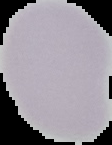
Summary:
  - Image size: 112×145 pixels
  - Preparation: thin blood film
  - Image type: cell region segmented out of the field of view; surrounding area masked to black
  - Malaria status: uninfected